Identify the parasite.
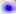
This is Toxoplasma gondii.

modality = micrograph
magnification = 400x